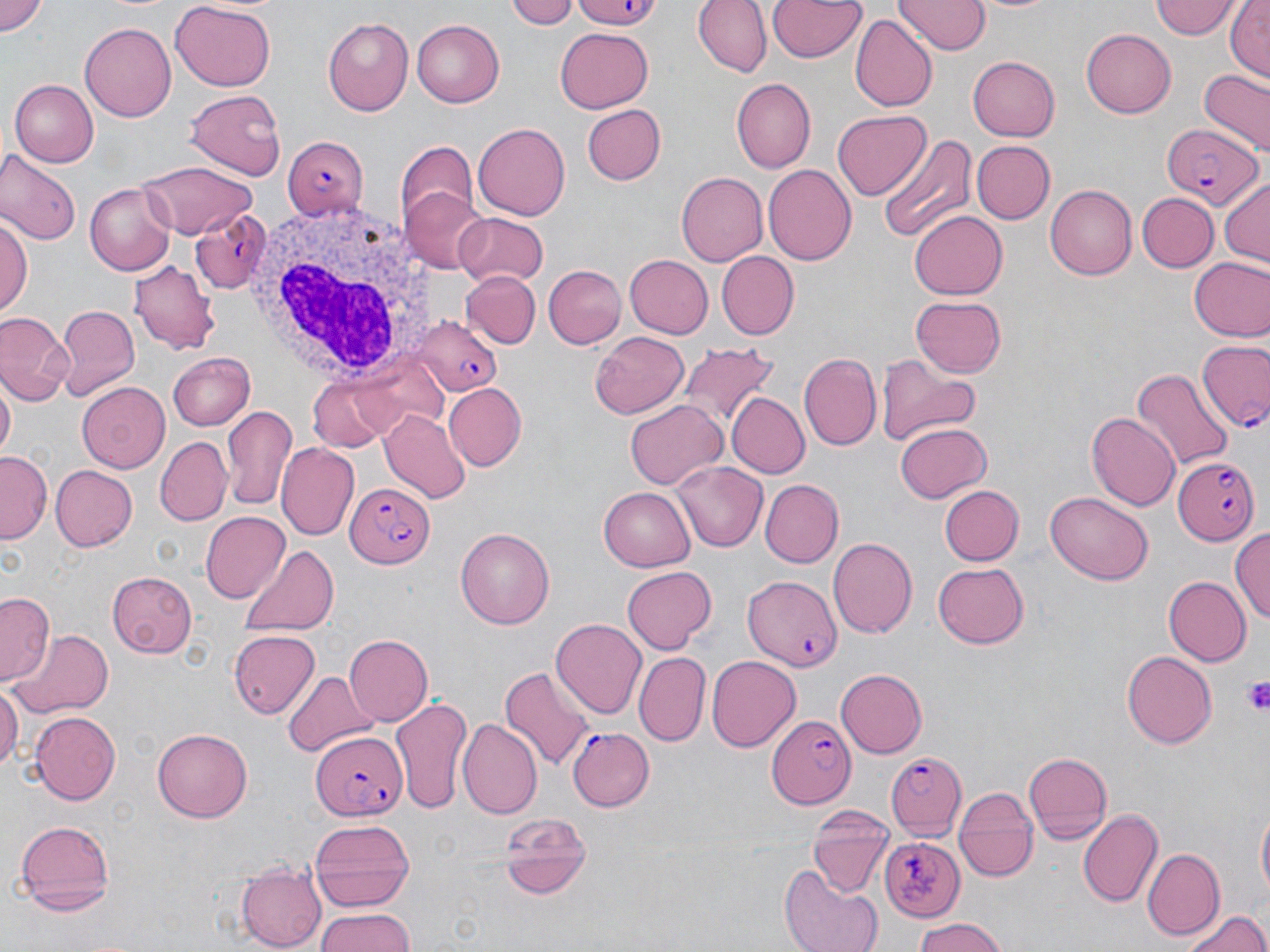
Summary:
  - Coordinate format: approximate bounding boxes as named x1/y1/x2/y2 corners in pixels
  - Plasmodium falciparum-infected red blood cell locations: (x1=1162, y1=120, x2=1262, y2=207), (x1=279, y1=136, x2=370, y2=220), (x1=188, y1=208, x2=274, y2=294), (x1=415, y1=318, x2=504, y2=396), (x1=1196, y1=337, x2=1270, y2=436), (x1=1171, y1=455, x2=1259, y2=546), (x1=342, y1=483, x2=433, y2=565), (x1=742, y1=575, x2=839, y2=678), (x1=767, y1=714, x2=858, y2=809), (x1=567, y1=726, x2=653, y2=811), (x1=308, y1=732, x2=404, y2=821), (x1=884, y1=748, x2=965, y2=841), (x1=883, y1=837, x2=964, y2=919)
  - Uninfected red blood cell locations: (x1=0, y1=0, x2=48, y2=37), (x1=506, y1=0, x2=582, y2=29), (x1=695, y1=0, x2=771, y2=77), (x1=766, y1=0, x2=866, y2=64), (x1=896, y1=0, x2=989, y2=56), (x1=1150, y1=0, x2=1240, y2=41), (x1=1226, y1=1, x2=1269, y2=82), (x1=101, y1=2, x2=177, y2=16), (x1=168, y1=4, x2=278, y2=90), (x1=851, y1=14, x2=938, y2=112), (x1=322, y1=17, x2=415, y2=116), (x1=81, y1=19, x2=176, y2=122), (x1=411, y1=19, x2=505, y2=108), (x1=553, y1=26, x2=653, y2=114), (x1=1082, y1=27, x2=1179, y2=117), (x1=967, y1=55, x2=1061, y2=141), (x1=1199, y1=68, x2=1269, y2=152), (x1=730, y1=78, x2=813, y2=172), (x1=9, y1=80, x2=98, y2=167), (x1=184, y1=88, x2=286, y2=179), (x1=580, y1=102, x2=669, y2=185), (x1=832, y1=110, x2=930, y2=201), (x1=473, y1=123, x2=569, y2=220), (x1=876, y1=132, x2=975, y2=243), (x1=969, y1=140, x2=1054, y2=225), (x1=395, y1=144, x2=478, y2=230), (x1=0, y1=155, x2=78, y2=247), (x1=137, y1=161, x2=257, y2=240), (x1=765, y1=164, x2=857, y2=265), (x1=675, y1=172, x2=767, y2=267), (x1=1220, y1=177, x2=1270, y2=267), (x1=85, y1=182, x2=175, y2=276), (x1=1044, y1=184, x2=1136, y2=280), (x1=399, y1=187, x2=490, y2=275), (x1=1139, y1=192, x2=1219, y2=272), (x1=909, y1=209, x2=1008, y2=300), (x1=2, y1=212, x2=32, y2=321), (x1=453, y1=212, x2=548, y2=287), (x1=714, y1=251, x2=799, y2=340), (x1=624, y1=254, x2=712, y2=339), (x1=1188, y1=257, x2=1270, y2=342), (x1=129, y1=261, x2=217, y2=352), (x1=543, y1=266, x2=626, y2=349), (x1=459, y1=271, x2=540, y2=349), (x1=911, y1=295, x2=1006, y2=379), (x1=55, y1=304, x2=140, y2=398), (x1=0, y1=313, x2=72, y2=405), (x1=591, y1=330, x2=689, y2=420), (x1=677, y1=343, x2=776, y2=436), (x1=167, y1=352, x2=256, y2=432), (x1=799, y1=353, x2=881, y2=453), (x1=878, y1=357, x2=980, y2=448), (x1=1132, y1=367, x2=1232, y2=477), (x1=307, y1=377, x2=402, y2=452), (x1=76, y1=381, x2=170, y2=471), (x1=442, y1=384, x2=526, y2=471), (x1=0, y1=385, x2=14, y2=461), (x1=67, y1=385, x2=155, y2=549), (x1=725, y1=392, x2=810, y2=479), (x1=625, y1=399, x2=728, y2=489), (x1=222, y1=405, x2=298, y2=510), (x1=381, y1=409, x2=471, y2=503), (x1=1087, y1=410, x2=1179, y2=509), (x1=897, y1=421, x2=992, y2=503), (x1=156, y1=437, x2=229, y2=525), (x1=277, y1=442, x2=359, y2=538), (x1=0, y1=452, x2=51, y2=540), (x1=671, y1=460, x2=769, y2=552), (x1=50, y1=464, x2=137, y2=551), (x1=759, y1=479, x2=843, y2=567), (x1=599, y1=485, x2=696, y2=570), (x1=940, y1=485, x2=1023, y2=565), (x1=1045, y1=493, x2=1154, y2=583), (x1=199, y1=511, x2=289, y2=602), (x1=1229, y1=526, x2=1270, y2=626), (x1=455, y1=527, x2=556, y2=629), (x1=827, y1=538, x2=917, y2=637), (x1=239, y1=545, x2=340, y2=637), (x1=933, y1=562, x2=1029, y2=649), (x1=622, y1=565, x2=716, y2=654), (x1=106, y1=570, x2=197, y2=657), (x1=1164, y1=577, x2=1250, y2=665), (x1=2, y1=593, x2=57, y2=684), (x1=549, y1=617, x2=646, y2=718), (x1=12, y1=627, x2=113, y2=717), (x1=228, y1=629, x2=322, y2=718), (x1=343, y1=635, x2=432, y2=726), (x1=1121, y1=648, x2=1216, y2=746), (x1=634, y1=652, x2=711, y2=745), (x1=707, y1=654, x2=801, y2=751), (x1=500, y1=666, x2=595, y2=773), (x1=835, y1=669, x2=927, y2=759), (x1=282, y1=672, x2=378, y2=758), (x1=0, y1=681, x2=22, y2=776), (x1=391, y1=694, x2=472, y2=813), (x1=28, y1=710, x2=118, y2=806), (x1=457, y1=718, x2=542, y2=821), (x1=153, y1=729, x2=249, y2=821), (x1=1022, y1=750, x2=1114, y2=842), (x1=952, y1=787, x2=1036, y2=883), (x1=1255, y1=800, x2=1269, y2=908), (x1=807, y1=808, x2=893, y2=896), (x1=1077, y1=808, x2=1162, y2=906), (x1=496, y1=809, x2=593, y2=898), (x1=12, y1=817, x2=116, y2=913), (x1=308, y1=817, x2=415, y2=908), (x1=1143, y1=848, x2=1224, y2=940), (x1=237, y1=863, x2=326, y2=949), (x1=779, y1=863, x2=885, y2=952), (x1=314, y1=906, x2=415, y2=952), (x1=1182, y1=909, x2=1269, y2=952), (x1=909, y1=919, x2=1012, y2=952)
  - Platelet locations: (x1=575, y1=0, x2=669, y2=28), (x1=1244, y1=677, x2=1270, y2=716)
  - White blood cell locations: (x1=244, y1=196, x2=446, y2=392)
  - Slide-level diagnosis: Plasmodium falciparum
  - Preparation: thin blood smear
  - Modality: light microscopy
  - Field of view: one of a larger specimen
  - Magnification: 1000x
  - Stain: May-Grünwald-Giemsa
  - Image size: 1270×952 pixels